Identify the parasite.
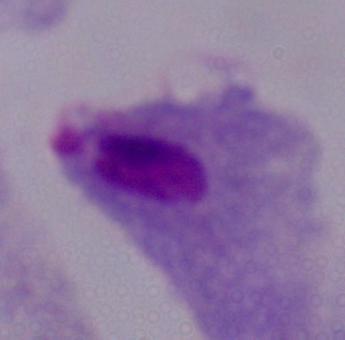

A trichomonad.

Micrograph. Captured at 1000x magnification.